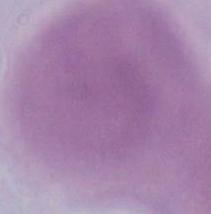

Summary:
  - Identification: erythrocyte
  - Magnification: 1000x
  - Modality: photomicrograph